Name the blood parasite species.
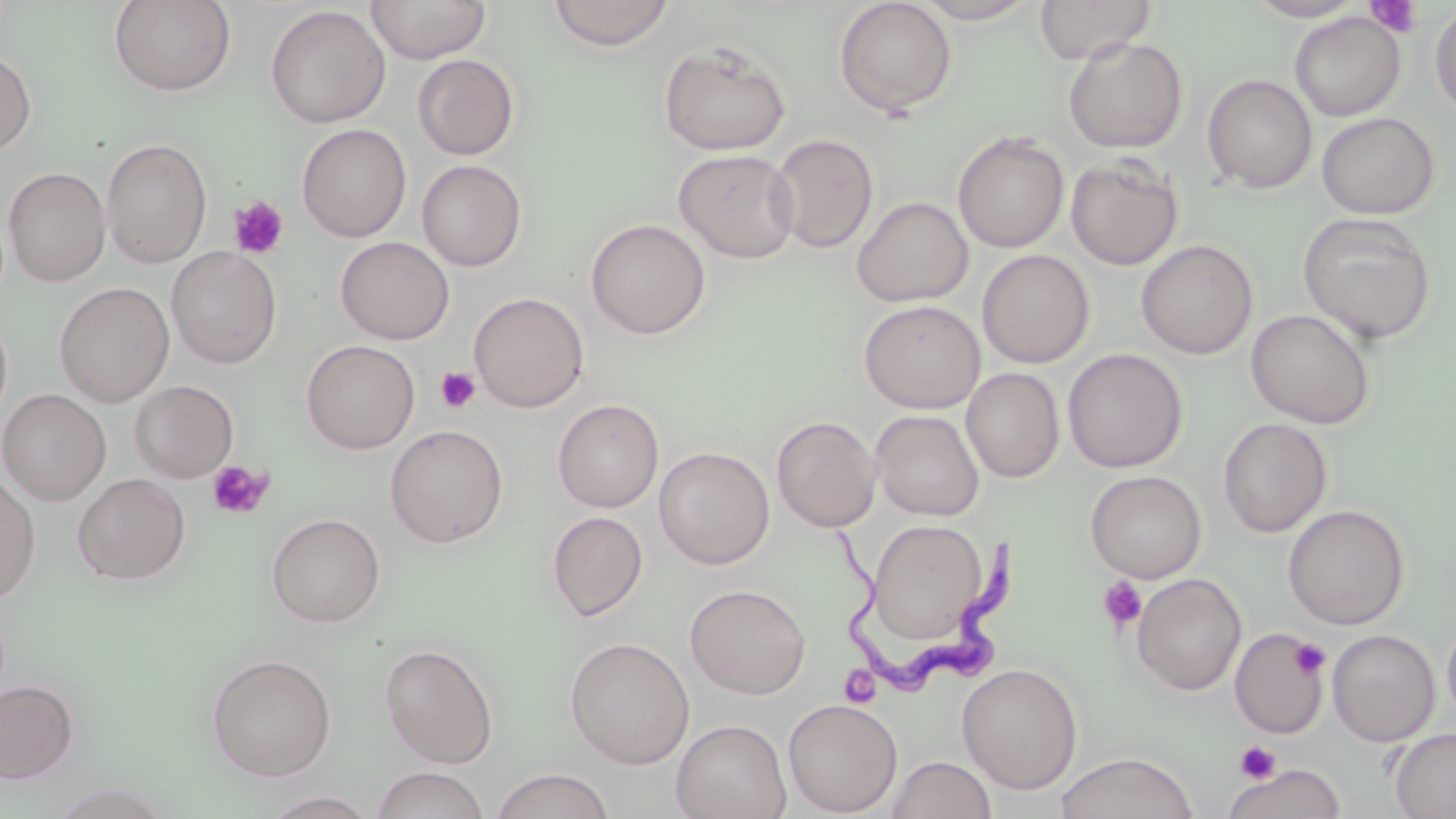
Trypanosoma brucei.

Summary:
  - Coordinate format: approximate bounding boxes as named x1/y1/x2/y2 corners in pixels
  - Uninfected red blood cell locations (subset): (x1=108, y1=0, x2=236, y2=96), (x1=366, y1=0, x2=491, y2=64), (x1=833, y1=0, x2=958, y2=118), (x1=914, y1=0, x2=1039, y2=24), (x1=1034, y1=0, x2=1157, y2=65), (x1=1245, y1=0, x2=1368, y2=21), (x1=545, y1=1, x2=677, y2=51), (x1=1430, y1=4, x2=1456, y2=120), (x1=265, y1=5, x2=390, y2=128), (x1=1289, y1=12, x2=1405, y2=121), (x1=1063, y1=36, x2=1188, y2=153), (x1=658, y1=40, x2=792, y2=156), (x1=0, y1=49, x2=37, y2=156), (x1=412, y1=54, x2=520, y2=160), (x1=1202, y1=74, x2=1317, y2=194), (x1=1316, y1=112, x2=1439, y2=219), (x1=296, y1=124, x2=412, y2=243), (x1=952, y1=131, x2=1069, y2=253), (x1=769, y1=133, x2=878, y2=254), (x1=101, y1=137, x2=212, y2=269), (x1=673, y1=149, x2=800, y2=264), (x1=1065, y1=155, x2=1184, y2=270), (x1=416, y1=160, x2=527, y2=271), (x1=3, y1=167, x2=111, y2=286), (x1=851, y1=196, x2=973, y2=307), (x1=1296, y1=212, x2=1438, y2=345), (x1=585, y1=219, x2=711, y2=340), (x1=336, y1=237, x2=454, y2=345), (x1=1136, y1=240, x2=1258, y2=359), (x1=167, y1=246, x2=283, y2=368), (x1=976, y1=250, x2=1094, y2=368), (x1=54, y1=282, x2=174, y2=407), (x1=469, y1=292, x2=590, y2=413), (x1=858, y1=300, x2=985, y2=413), (x1=1245, y1=308, x2=1376, y2=429), (x1=0, y1=309, x2=13, y2=428), (x1=301, y1=340, x2=420, y2=454), (x1=1063, y1=348, x2=1188, y2=473), (x1=961, y1=367, x2=1065, y2=482), (x1=130, y1=380, x2=238, y2=482), (x1=0, y1=389, x2=111, y2=505), (x1=552, y1=398, x2=664, y2=513), (x1=870, y1=409, x2=984, y2=521), (x1=771, y1=415, x2=881, y2=533), (x1=1218, y1=418, x2=1332, y2=538), (x1=385, y1=424, x2=509, y2=548), (x1=654, y1=446, x2=775, y2=570), (x1=1085, y1=470, x2=1206, y2=583), (x1=73, y1=472, x2=191, y2=585), (x1=0, y1=475, x2=41, y2=605), (x1=1283, y1=504, x2=1410, y2=630), (x1=547, y1=511, x2=648, y2=621), (x1=265, y1=513, x2=385, y2=629), (x1=866, y1=518, x2=992, y2=646), (x1=1131, y1=573, x2=1246, y2=696), (x1=685, y1=583, x2=811, y2=700), (x1=1441, y1=616, x2=1456, y2=727), (x1=1327, y1=629, x2=1440, y2=747), (x1=565, y1=637, x2=696, y2=769), (x1=380, y1=643, x2=499, y2=767), (x1=205, y1=652, x2=337, y2=781), (x1=957, y1=662, x2=1083, y2=794), (x1=0, y1=678, x2=80, y2=784), (x1=783, y1=698, x2=903, y2=816), (x1=671, y1=718, x2=792, y2=819), (x1=1389, y1=727, x2=1456, y2=818), (x1=1053, y1=752, x2=1199, y2=819), (x1=885, y1=755, x2=997, y2=819), (x1=1222, y1=763, x2=1346, y2=819), (x1=370, y1=766, x2=491, y2=819), (x1=489, y1=769, x2=615, y2=819), (x1=260, y1=790, x2=380, y2=818)
  - Trypanosoma brucei locations: (x1=834, y1=513, x2=1020, y2=695)
  - Platelet locations (subset): (x1=1364, y1=1, x2=1423, y2=38), (x1=228, y1=195, x2=289, y2=260), (x1=435, y1=366, x2=481, y2=413), (x1=206, y1=461, x2=274, y2=521), (x1=1098, y1=575, x2=1147, y2=631), (x1=1289, y1=638, x2=1331, y2=680), (x1=839, y1=666, x2=880, y2=708), (x1=1235, y1=740, x2=1281, y2=783), (x1=1220, y1=754, x2=1313, y2=810)
  - Magnification: 1000x
  - Preparation: thin blood film
  - Field of view: one of a larger specimen
  - Image size: 1456×819 pixels
  - Stain: May-Grünwald-Giemsa
  - Modality: light microscopy